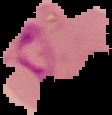

Summary:
  - Malaria status: parasitized
  - Preparation: thin blood smear
  - Image size: 112×115 pixels
  - Image type: segmented cell region with the area outside set to black